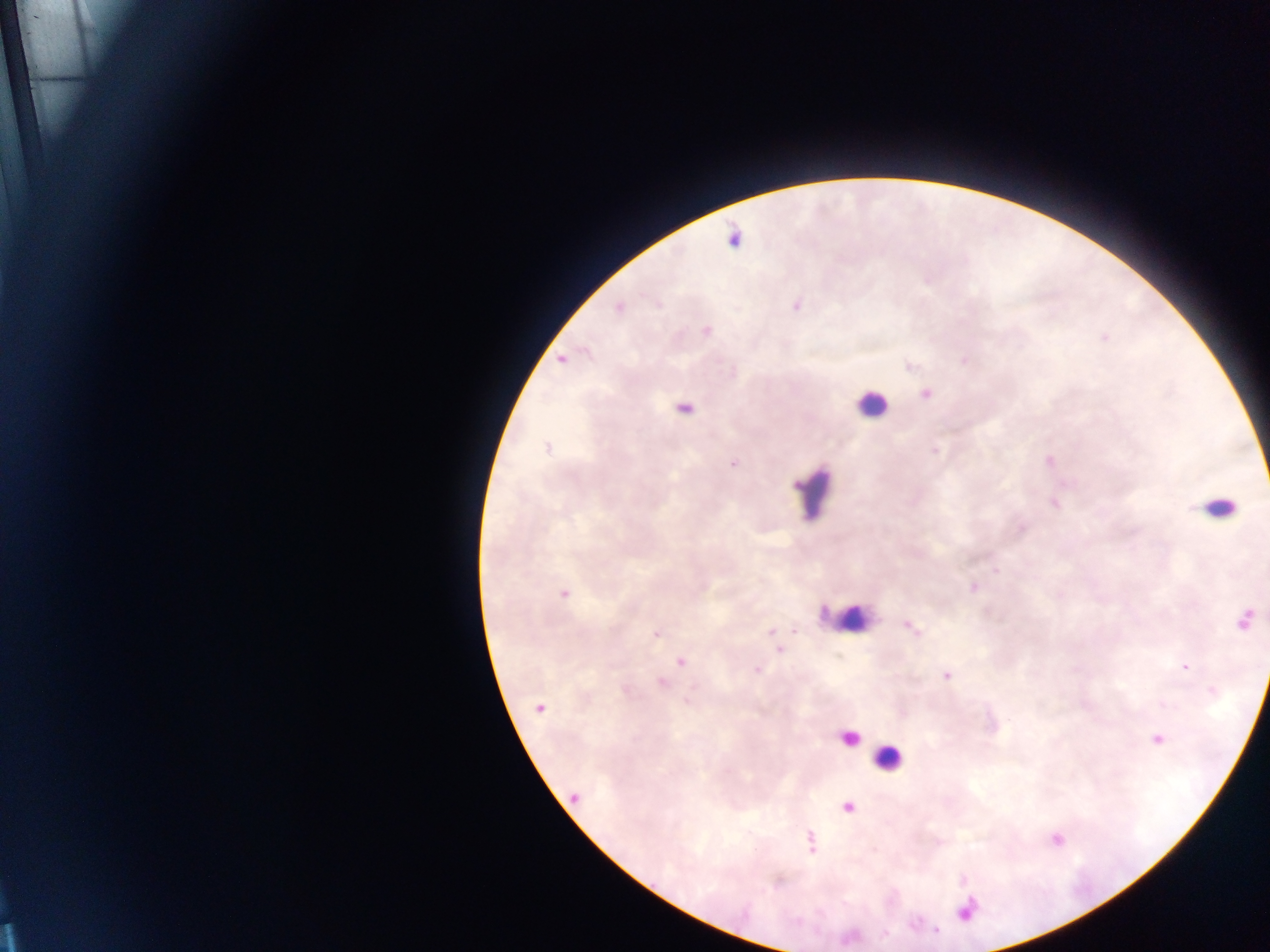

Approximate centers as [x, y] in pixels.
Summary:
  - Leukocyte locations: [871, 404], [813, 491], [1217, 508], [852, 618], [846, 738], [888, 758]
  - Malaria parasite locations: [734, 239], [796, 305], [618, 308], [707, 330], [562, 359], [925, 394], [685, 408], [547, 447], [935, 451], [734, 463], [997, 571], [973, 588], [563, 594], [1246, 619], [913, 628], [656, 634], [680, 662], [1185, 667], [757, 670], [947, 675], [662, 682], [538, 708], [1158, 738], [575, 797], [847, 807], [811, 841], [965, 912]
  - Preparation: thick blood smear
  - Capture: mobile-phone photograph through a microscope
  - Field of view: single
  - Country: Ghana
  - Image size: 1270×952 pixels